State which cell type is depicted.
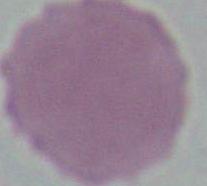
An erythrocyte.

1000x magnification. Micrograph.